Assess this cell for malaria.
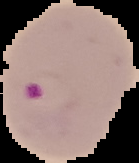
Parasitized.

{
  "preparation": "thin blood smear",
  "image_type": "cell region segmented out of the field of view; surrounding area masked to black",
  "image_size": "139×163 pixels"
}